Classify this cell by malaria status.
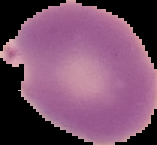

Parasitized.

Segmented cell region on a black background. Image is 157×145 pixels. From a thin blood film.